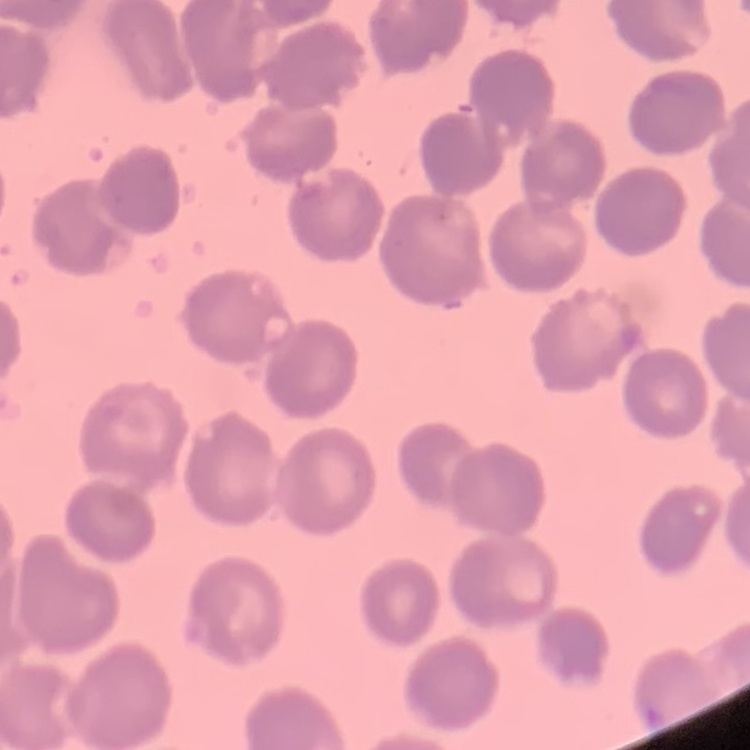

The erythrocytes exhibit no rouleaux formation. Square crop of a larger photomicrograph. Field's or Giemsa stain. Thin blood film.